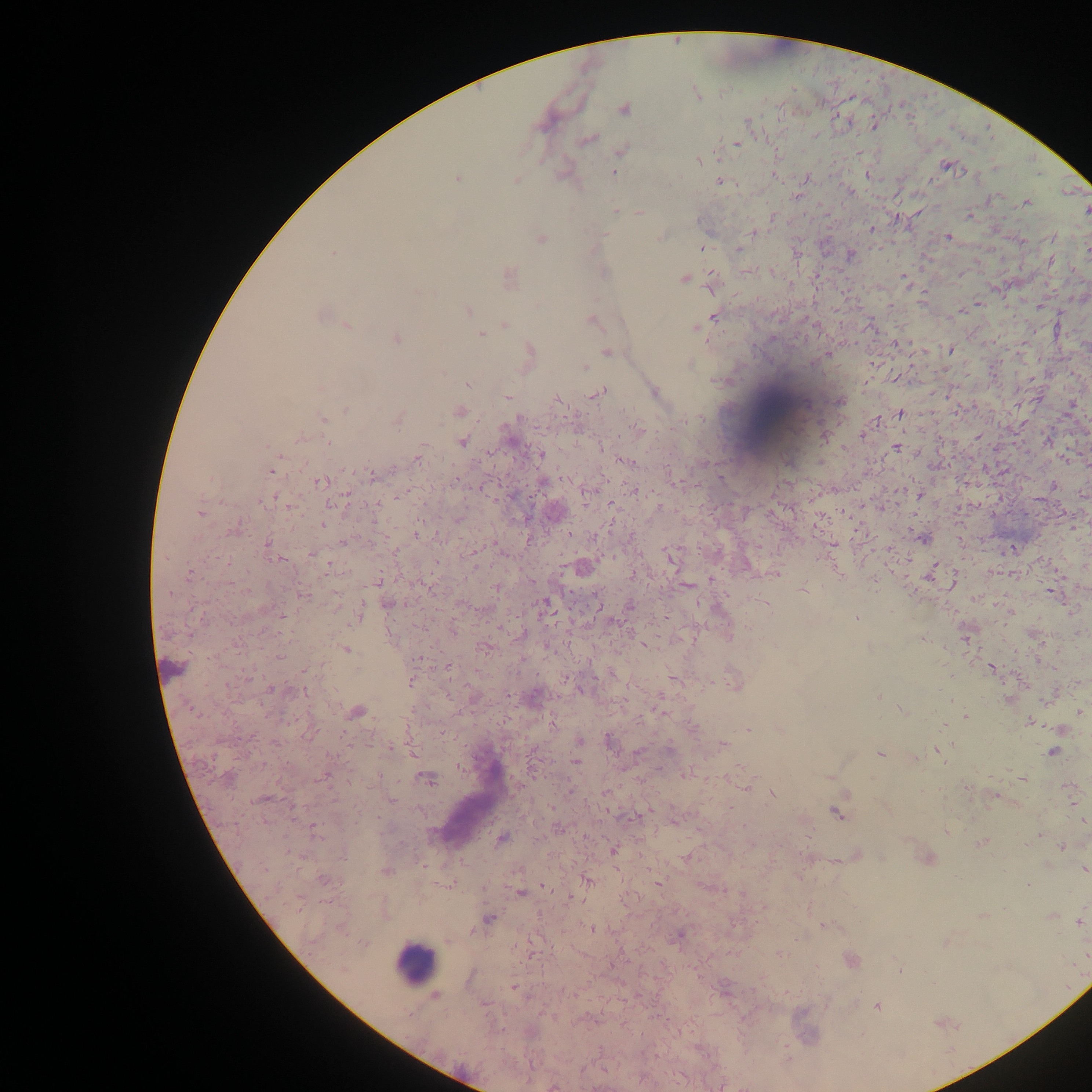

Approximate centers as [x, y] in pixels.
Summary:
  - Malaria parasite locations: [696, 94], [624, 109], [748, 122], [875, 124], [588, 139], [737, 143], [620, 151], [700, 161], [946, 166], [614, 172], [868, 175], [458, 178], [515, 180], [720, 181], [849, 191], [1026, 202], [1087, 210], [616, 211], [640, 212], [969, 216], [871, 229], [753, 232], [661, 236], [1052, 237], [948, 238], [541, 239], [1021, 241], [702, 248], [738, 249], [1087, 249], [333, 253], [850, 255], [1050, 262], [746, 272], [604, 273], [509, 277], [684, 279], [711, 282], [468, 310], [960, 311], [714, 317], [592, 320], [504, 325], [347, 326], [696, 329], [480, 335], [397, 339], [897, 343], [529, 350], [950, 351], [606, 352], [827, 354], [584, 367], [467, 384], [321, 388], [600, 392], [655, 393], [508, 397], [556, 399], [840, 402], [347, 409], [461, 411], [900, 414], [323, 418], [519, 418], [399, 420], [639, 430], [864, 435], [978, 437], [299, 439], [1047, 441], [462, 443], [601, 446], [896, 447], [541, 455], [417, 458], [627, 461], [272, 470], [373, 475], [456, 480], [321, 482], [543, 484], [1052, 485], [398, 497], [272, 499], [266, 500], [332, 504], [612, 505], [658, 508], [199, 512], [322, 525], [234, 530], [418, 533], [570, 535], [923, 538], [342, 542], [268, 544], [312, 553], [670, 556], [280, 560], [189, 574], [929, 574], [634, 575], [378, 580], [953, 581], [688, 586], [429, 589], [495, 589], [803, 590], [170, 594], [1053, 594], [304, 595], [336, 600], [544, 604], [390, 605], [630, 607], [282, 616], [356, 618], [856, 619], [454, 630], [523, 635], [965, 636], [869, 647], [484, 648], [346, 650], [279, 656], [418, 659], [448, 666], [992, 669], [411, 683], [734, 684], [227, 685], [272, 689], [305, 691], [879, 695], [535, 696], [1008, 699], [191, 710], [903, 711], [357, 712], [1080, 712], [965, 717], [1029, 722], [748, 729], [780, 729], [1059, 729], [608, 740], [579, 741], [276, 743], [722, 745], [390, 747], [670, 750], [936, 750], [638, 752], [1053, 752], [880, 754], [576, 762], [324, 777], [829, 778], [427, 779], [1022, 779], [747, 786], [569, 788], [606, 792], [772, 794], [264, 799], [391, 800], [837, 813], [264, 822], [1084, 822], [558, 828], [316, 829], [947, 832], [1040, 834], [501, 839], [982, 842], [1060, 846], [614, 851], [686, 858], [423, 867], [1085, 870], [387, 872], [323, 879], [587, 881], [1028, 885], [543, 886], [521, 893], [1053, 916], [489, 919], [1080, 922], [591, 929], [679, 936], [362, 942], [447, 942], [779, 954], [850, 960], [900, 970], [513, 987], [435, 996], [877, 1007], [553, 1087]
  - Leukocyte locations: [414, 962]
  - Preparation: thick blood film
  - Field of view: single
  - Capture: mobile-phone photograph through a microscope
  - Image size: 1092×1092 pixels
  - Country: Ghana